Outline platelets.
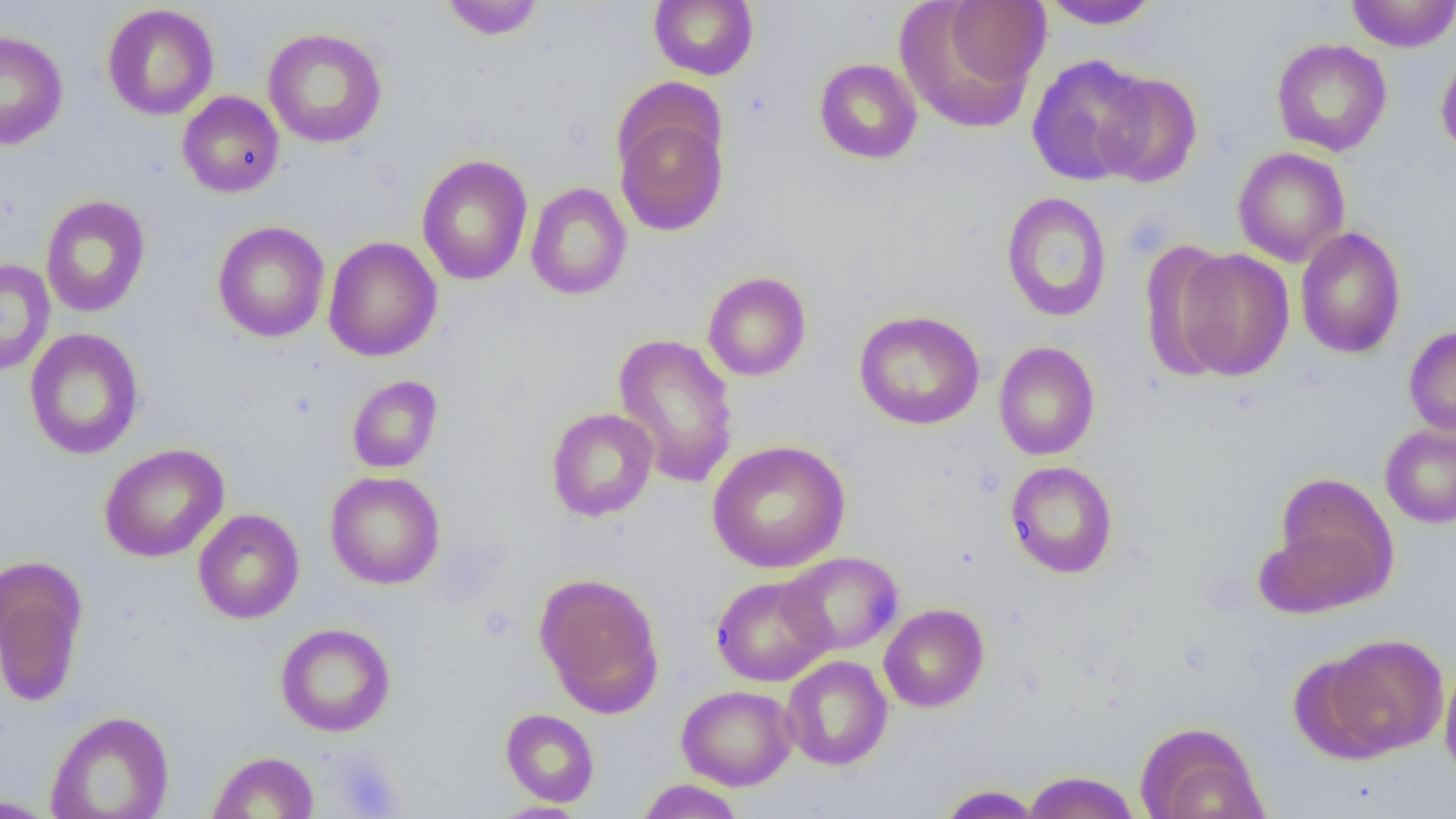
Approximate bounding boxes as (x1, y1, x2, y2) in pixels.
Platelets: (332, 751, 405, 818).

Summary:
  - Uninfected red blood cell locations: (440, 0, 544, 40), (649, 0, 758, 80), (1346, 0, 1456, 52), (1040, 1, 1162, 30), (895, 3, 1044, 131), (102, 4, 219, 120), (263, 28, 387, 148), (0, 29, 68, 151), (1271, 38, 1392, 157), (1436, 45, 1456, 159), (1026, 54, 1154, 187), (813, 58, 922, 164), (1093, 72, 1203, 187), (177, 91, 284, 198), (614, 108, 729, 236), (1232, 147, 1350, 267), (416, 154, 533, 285), (525, 182, 632, 300), (1001, 192, 1112, 322), (40, 195, 150, 317), (212, 221, 330, 342), (1295, 227, 1406, 358), (324, 236, 443, 362), (1138, 239, 1237, 380), (1171, 248, 1295, 381), (0, 259, 55, 375), (703, 271, 812, 381), (853, 309, 984, 430), (1404, 325, 1456, 436), (23, 328, 144, 460), (612, 333, 739, 489), (993, 341, 1101, 460), (347, 375, 443, 473), (545, 407, 659, 522), (1379, 423, 1456, 529), (707, 440, 850, 573), (99, 443, 229, 562), (1005, 460, 1119, 578), (325, 471, 445, 589), (1271, 471, 1396, 587), (193, 508, 304, 624), (1254, 519, 1392, 619), (779, 551, 904, 656), (0, 558, 88, 708), (534, 572, 665, 714), (711, 575, 832, 687), (879, 603, 989, 712), (275, 623, 396, 737), (1316, 633, 1449, 759), (781, 655, 893, 770), (1439, 662, 1456, 784), (677, 684, 797, 791), (500, 708, 599, 807), (45, 709, 175, 819), (1134, 721, 1268, 819), (207, 751, 319, 818), (1022, 771, 1140, 819), (636, 779, 744, 819), (937, 784, 1043, 818), (0, 796, 59, 818), (487, 801, 589, 818)
  - Slide-level diagnosis: no evidence of blood parasites
  - Image size: 1456×819 pixels
  - Field of view: one of a larger specimen
  - Magnification: 1000x
  - Preparation: thin blood smear
  - Modality: optical microscopy